Outline each Plasmodium malariae-infected red blood cell.
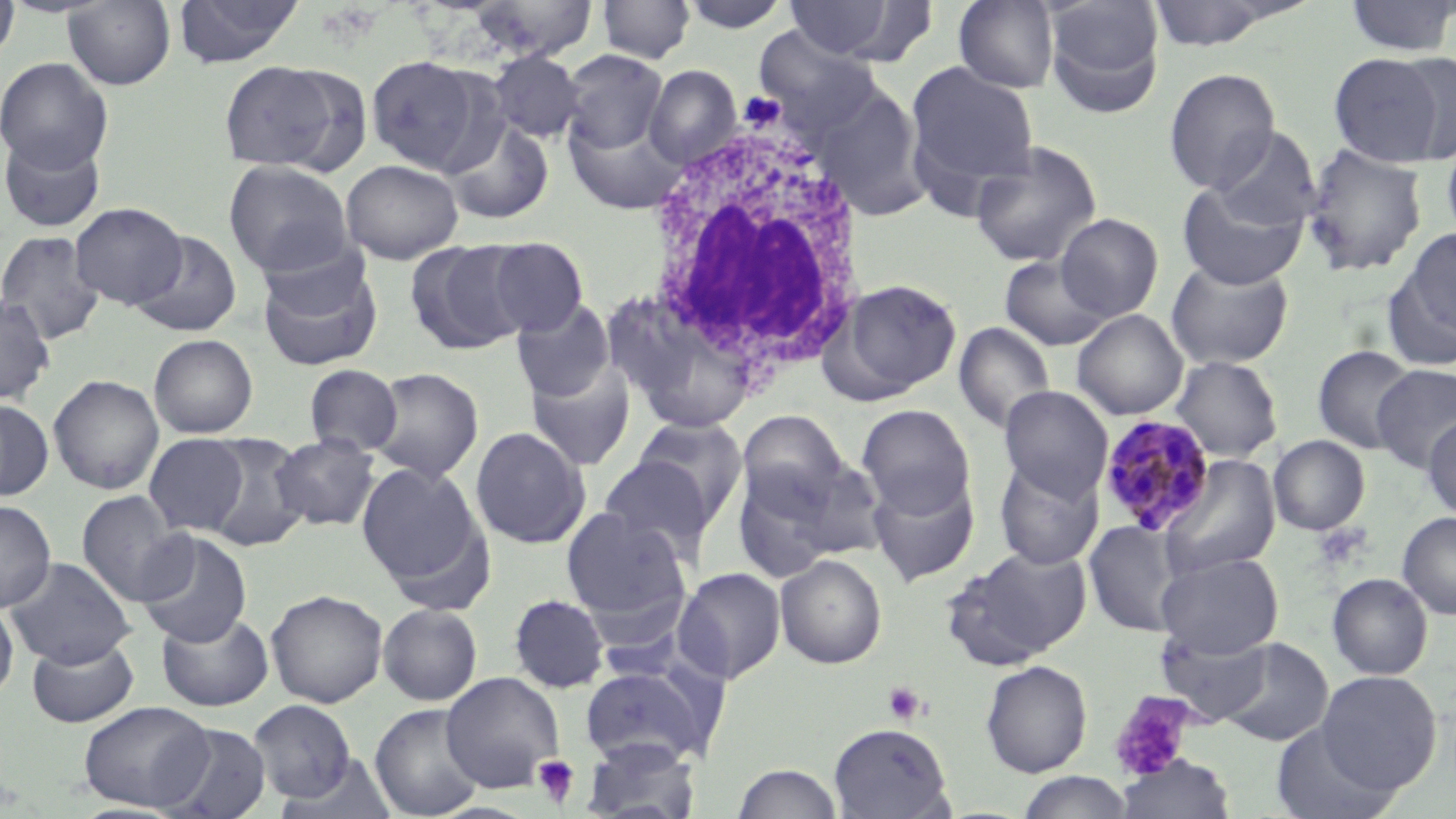

Approximate bounding boxes as named x1/y1/x2/y2 corners in pixels.
Plasmodium malariae-infected red blood cells: (x1=1099, y1=415, x2=1215, y2=536).

Platelet locations: (x1=884, y1=681, x2=928, y2=725), (x1=1109, y1=691, x2=1195, y2=781), (x1=532, y1=755, x2=580, y2=808). Uninfected red blood cell locations: (x1=0, y1=0, x2=20, y2=70), (x1=62, y1=0, x2=177, y2=89), (x1=172, y1=0, x2=305, y2=68), (x1=464, y1=0, x2=599, y2=62), (x1=597, y1=0, x2=696, y2=63), (x1=678, y1=0, x2=793, y2=33), (x1=779, y1=0, x2=933, y2=64), (x1=953, y1=0, x2=1059, y2=92), (x1=1043, y1=0, x2=1166, y2=116), (x1=1142, y1=0, x2=1293, y2=52), (x1=1342, y1=0, x2=1456, y2=57), (x1=560, y1=49, x2=668, y2=155), (x1=486, y1=50, x2=585, y2=143), (x1=1329, y1=50, x2=1452, y2=167), (x1=365, y1=54, x2=494, y2=175), (x1=0, y1=56, x2=113, y2=172), (x1=218, y1=59, x2=353, y2=173), (x1=905, y1=62, x2=1040, y2=196), (x1=644, y1=64, x2=741, y2=168), (x1=1164, y1=68, x2=1281, y2=193), (x1=816, y1=85, x2=930, y2=222), (x1=564, y1=109, x2=687, y2=215), (x1=443, y1=118, x2=554, y2=226), (x1=1209, y1=128, x2=1321, y2=232), (x1=1441, y1=132, x2=1456, y2=244), (x1=0, y1=134, x2=106, y2=233), (x1=969, y1=140, x2=1102, y2=267), (x1=1301, y1=143, x2=1428, y2=277), (x1=342, y1=159, x2=463, y2=264), (x1=223, y1=160, x2=354, y2=278), (x1=1176, y1=179, x2=1308, y2=290), (x1=69, y1=202, x2=187, y2=309), (x1=1056, y1=213, x2=1163, y2=321), (x1=1398, y1=225, x2=1456, y2=349), (x1=0, y1=230, x2=105, y2=345), (x1=131, y1=230, x2=243, y2=337), (x1=482, y1=236, x2=589, y2=338), (x1=406, y1=239, x2=530, y2=355), (x1=999, y1=255, x2=1116, y2=351), (x1=257, y1=257, x2=383, y2=371), (x1=1165, y1=259, x2=1294, y2=370), (x1=827, y1=278, x2=962, y2=401), (x1=0, y1=294, x2=56, y2=405), (x1=611, y1=296, x2=763, y2=434), (x1=511, y1=299, x2=616, y2=402), (x1=1072, y1=310, x2=1188, y2=420), (x1=953, y1=322, x2=1057, y2=435), (x1=148, y1=334, x2=258, y2=438), (x1=1312, y1=345, x2=1418, y2=454), (x1=1170, y1=356, x2=1283, y2=463), (x1=525, y1=359, x2=637, y2=471), (x1=304, y1=364, x2=403, y2=456), (x1=1372, y1=364, x2=1456, y2=473), (x1=368, y1=367, x2=484, y2=483), (x1=47, y1=374, x2=165, y2=495), (x1=999, y1=386, x2=1113, y2=501), (x1=0, y1=398, x2=54, y2=503), (x1=856, y1=404, x2=975, y2=518), (x1=737, y1=410, x2=851, y2=517), (x1=1423, y1=413, x2=1456, y2=521), (x1=632, y1=416, x2=749, y2=529), (x1=470, y1=426, x2=590, y2=549), (x1=144, y1=433, x2=249, y2=536), (x1=201, y1=434, x2=312, y2=553), (x1=271, y1=434, x2=380, y2=531), (x1=1269, y1=435, x2=1370, y2=535), (x1=598, y1=456, x2=712, y2=561), (x1=1159, y1=456, x2=1280, y2=579), (x1=994, y1=457, x2=1103, y2=570), (x1=356, y1=462, x2=486, y2=592), (x1=731, y1=462, x2=844, y2=584), (x1=867, y1=471, x2=979, y2=586), (x1=75, y1=490, x2=191, y2=607), (x1=0, y1=499, x2=56, y2=613), (x1=561, y1=507, x2=690, y2=622), (x1=1397, y1=512, x2=1456, y2=619), (x1=1084, y1=520, x2=1186, y2=637), (x1=135, y1=530, x2=252, y2=646), (x1=941, y1=545, x2=1092, y2=670), (x1=1155, y1=552, x2=1283, y2=658), (x1=775, y1=554, x2=887, y2=669), (x1=4, y1=556, x2=136, y2=668), (x1=674, y1=566, x2=786, y2=684), (x1=1327, y1=572, x2=1433, y2=680), (x1=265, y1=588, x2=388, y2=707), (x1=508, y1=594, x2=609, y2=694), (x1=0, y1=599, x2=19, y2=703), (x1=378, y1=603, x2=482, y2=705), (x1=156, y1=610, x2=273, y2=712), (x1=1156, y1=627, x2=1275, y2=723), (x1=26, y1=636, x2=139, y2=728), (x1=1215, y1=637, x2=1334, y2=746), (x1=980, y1=660, x2=1093, y2=777), (x1=578, y1=662, x2=721, y2=768), (x1=1316, y1=670, x2=1441, y2=794), (x1=441, y1=672, x2=564, y2=792), (x1=249, y1=699, x2=357, y2=803), (x1=78, y1=701, x2=213, y2=812), (x1=370, y1=703, x2=485, y2=819), (x1=1270, y1=720, x2=1401, y2=819), (x1=156, y1=722, x2=273, y2=819), (x1=828, y1=722, x2=954, y2=818), (x1=581, y1=739, x2=702, y2=818), (x1=278, y1=753, x2=399, y2=819), (x1=1116, y1=754, x2=1236, y2=819), (x1=732, y1=763, x2=843, y2=819), (x1=1017, y1=772, x2=1135, y2=818). White blood cell locations: (x1=644, y1=115, x2=871, y2=381). Slide-level diagnosis: Plasmodium malariae. Thin blood film. May-Grünwald-Giemsa-stained preparation. Captured at 1000x magnification. Single field of view. Image is 1456×819 pixels. Light microscopy.